Identify the parasite.
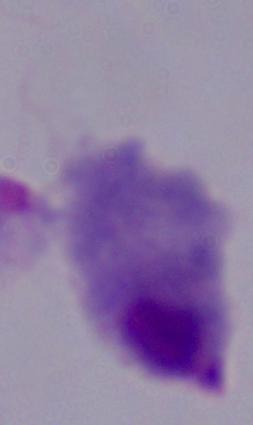
This is a trichomonad.

magnification = 1000x
modality = micrograph